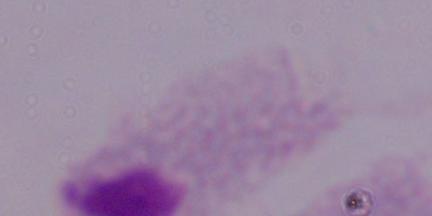

Summary:
  - Modality: photomicrograph
  - Magnification: 1000x
  - Identification: trichomonad